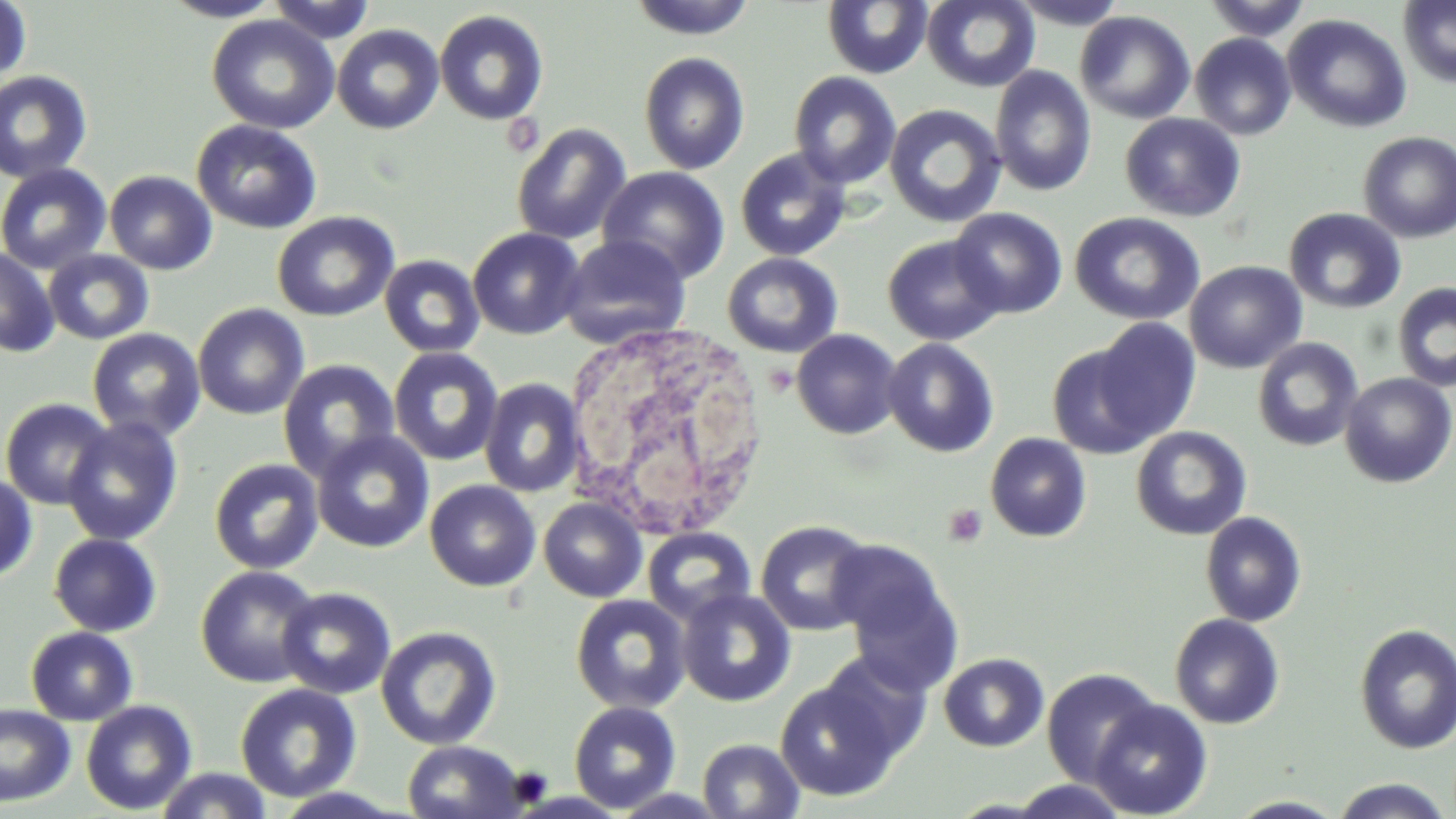

Summary:
  - Coordinate format: approximate bounding boxes as (x1, y1, x2, y2) in pixels
  - White blood cell locations: (564, 321, 760, 532)
  - Platelet locations: (504, 113, 544, 158), (943, 503, 988, 548)
  - Uninfected red blood cell locations: (158, 0, 285, 21), (268, 0, 377, 44), (627, 0, 758, 40), (921, 0, 1040, 92), (1008, 0, 1131, 29), (1203, 0, 1312, 41), (0, 1, 32, 88), (822, 1, 932, 79), (1398, 1, 1456, 89), (434, 10, 548, 125), (1075, 10, 1196, 124), (1282, 13, 1412, 133), (206, 15, 340, 134), (331, 24, 444, 135), (1190, 33, 1296, 140), (638, 52, 750, 175), (990, 66, 1096, 197), (0, 70, 94, 184), (788, 71, 902, 189), (884, 103, 1007, 228), (499, 111, 546, 157), (1120, 113, 1246, 222), (191, 119, 322, 234), (511, 123, 632, 245), (1358, 131, 1456, 243), (735, 148, 851, 261), (0, 163, 112, 275), (598, 166, 730, 284), (104, 170, 217, 275), (949, 207, 1068, 319), (1284, 207, 1406, 314), (272, 211, 399, 322), (1070, 212, 1205, 326), (468, 227, 585, 340), (558, 235, 692, 348), (882, 235, 1005, 346), (0, 246, 59, 357), (42, 249, 155, 345), (722, 252, 843, 358), (379, 254, 485, 358), (1184, 260, 1307, 374), (1392, 282, 1456, 392), (193, 302, 310, 420), (1091, 318, 1201, 443), (86, 327, 206, 443), (792, 329, 902, 439), (1252, 337, 1364, 452), (883, 338, 999, 457), (1047, 343, 1157, 459), (388, 347, 504, 467), (278, 359, 401, 481), (1339, 372, 1456, 487), (479, 378, 586, 498), (0, 398, 116, 510), (61, 416, 183, 546), (1131, 426, 1252, 540), (311, 430, 435, 554), (985, 433, 1092, 542), (209, 458, 324, 575), (0, 474, 38, 583), (425, 479, 541, 592), (538, 497, 647, 602), (1200, 511, 1307, 627), (755, 520, 875, 635), (642, 527, 757, 625), (48, 533, 162, 637), (830, 546, 963, 690), (195, 565, 322, 688), (276, 587, 396, 699), (676, 588, 796, 707), (570, 594, 691, 715), (1169, 613, 1285, 729), (1354, 623, 1456, 754), (26, 625, 138, 725), (376, 626, 501, 750), (815, 651, 933, 764), (938, 653, 1049, 752), (1039, 668, 1162, 784), (773, 674, 904, 801), (234, 682, 362, 803), (1088, 698, 1212, 818), (80, 699, 198, 814), (569, 701, 682, 813), (0, 703, 76, 807), (696, 738, 804, 818), (401, 740, 530, 819), (154, 767, 274, 819), (1330, 777, 1452, 818), (1001, 780, 1134, 818), (269, 787, 415, 818), (607, 788, 734, 818), (1226, 795, 1349, 818)
  - Slide-level diagnosis: no evidence of blood parasites
  - Preparation: thin blood film
  - Magnification: 1000x
  - Field of view: one of a larger specimen
  - Image size: 1456×819 pixels
  - Stain: May-Grünwald-Giemsa
  - Modality: optical microscopy